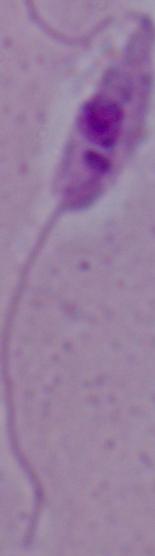

Summary:
  - Modality: photomicrograph
  - Magnification: 1000x
  - Identification: Leishmania